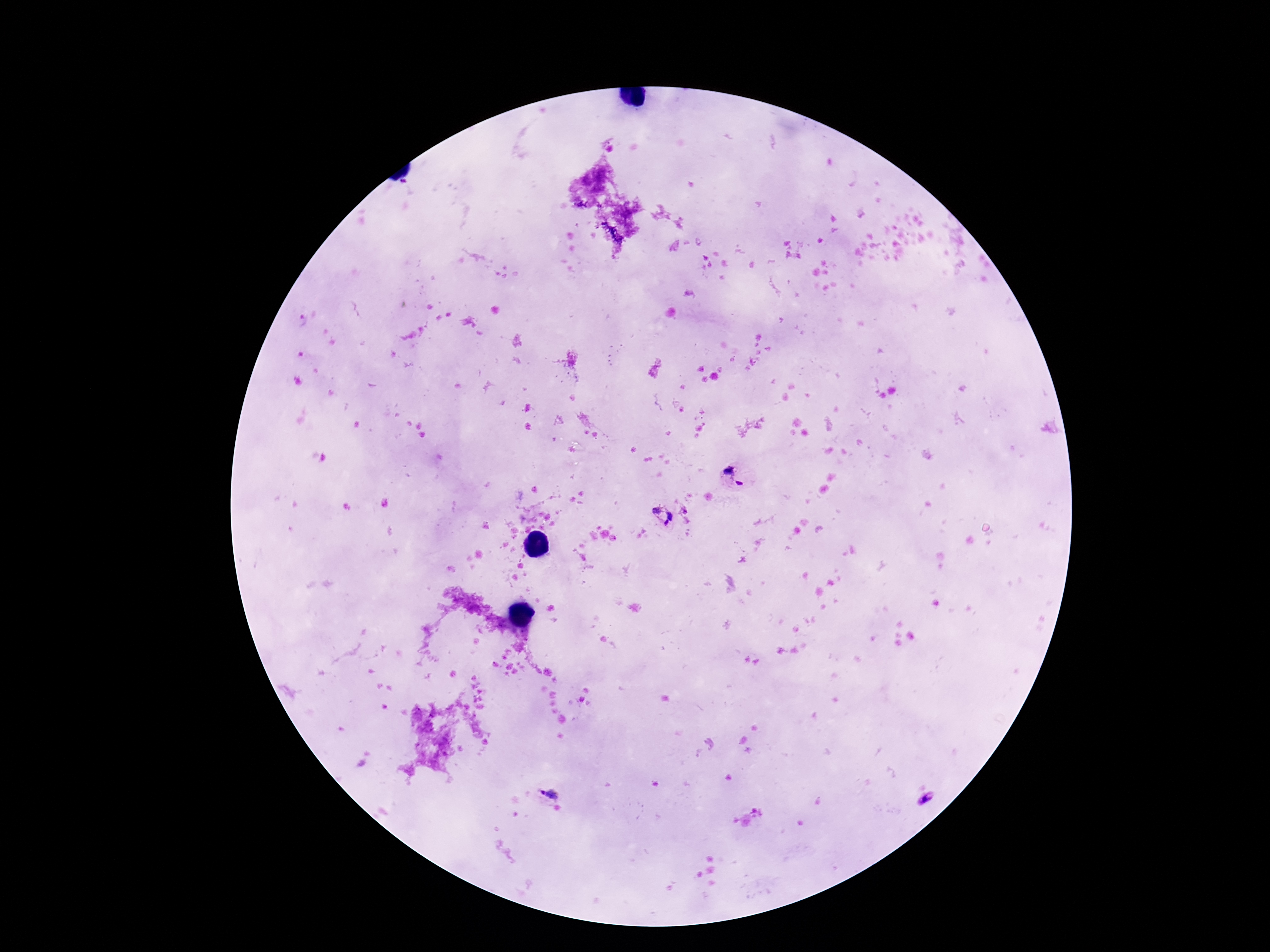
Approximate centers as (x, y) in pixels.
Summary:
  - Plasmodium parasite locations: (733, 477), (673, 515), (547, 794), (930, 803)
  - Patient malaria status: infected
  - Image size: 1270×952 pixels
  - Field of view: single
  - Capture: smartphone camera through the microscope eyepiece
  - Stain: Giemsa
  - Magnification: 100x
  - Preparation: thick blood smear